Classify this cell by malaria status.
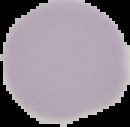
It is uninfected.

The area outside the segmented cell region is set to black. From a thin blood film. Image is 130×127 pixels.